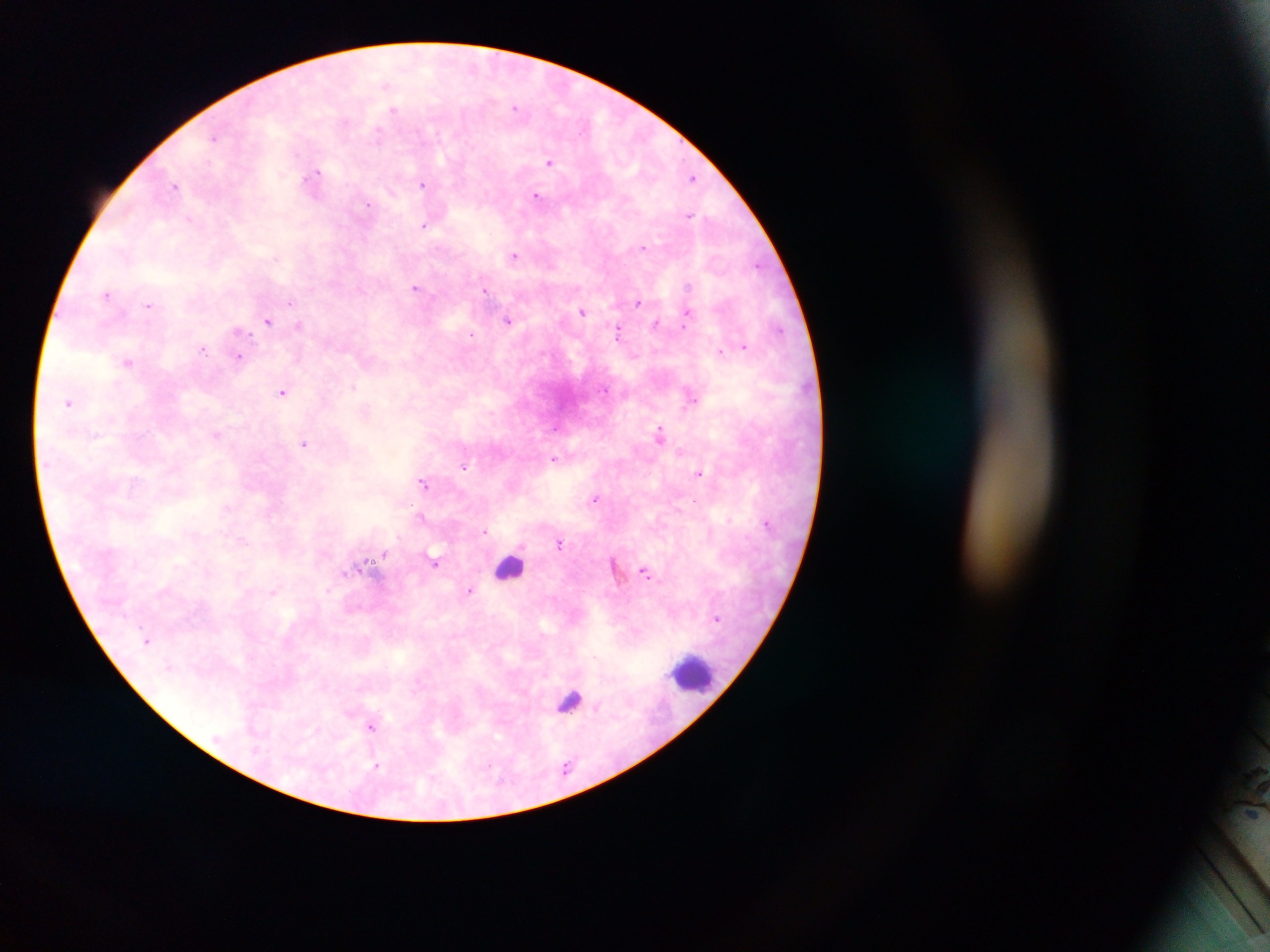
Approximate centers as x y in pixels.
Summary:
  - Malaria parasite locations: 387 86; 516 107; 394 111; 377 134; 214 137; 549 161; 315 175; 693 177; 423 184; 175 185; 536 196; 367 204; 690 214; 189 218; 424 225; 643 248; 514 255; 757 266; 688 286; 415 288; 484 290; 107 294; 638 302; 290 303; 148 304; 583 312; 687 313; 508 320; 268 321; 656 323; 299 324; 684 328; 779 329; 618 332; 241 333; 471 336; 745 346; 202 350; 721 351; 239 357; 127 361; 354 387; 282 392; 689 395; 69 403; 660 433; 216 434; 304 442; 554 459; 463 466; 700 473; 424 482; 595 498; 420 515; 730 520; 484 530; 243 540; 559 544; 384 554; 435 560; 645 573; 470 590; 273 591; 148 640; 570 701; 372 726; 376 766
  - Leukocyte locations: 509 566; 693 673
  - Country: Ghana
  - Field of view: single
  - Preparation: thick blood film
  - Image size: 1270×952 pixels
  - Capture: mobile-phone photograph through a microscope